Describe the morphology of the erythrocytes.
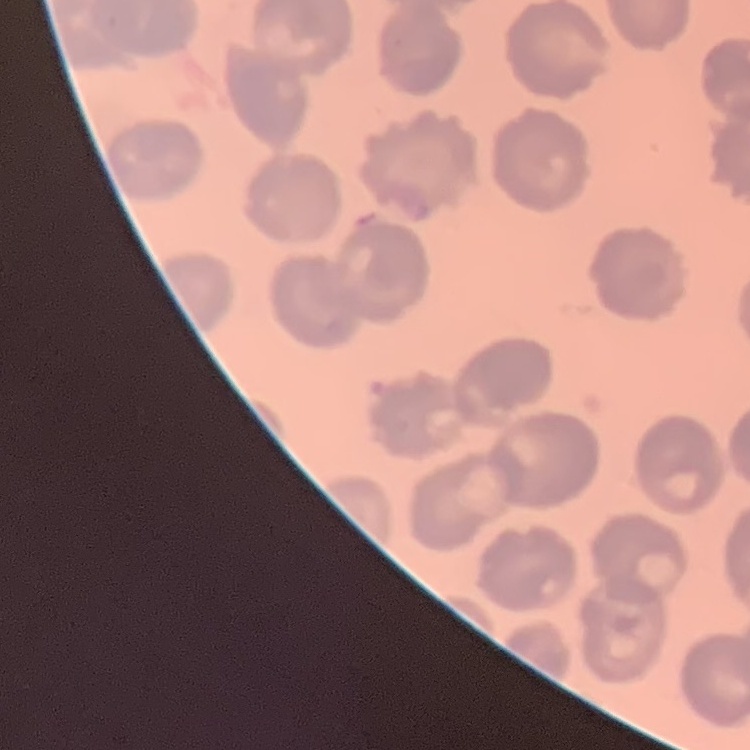

No rouleaux formation.

Field's or Giemsa stain. Thin blood smear. One tile cut from a larger photomicrograph.